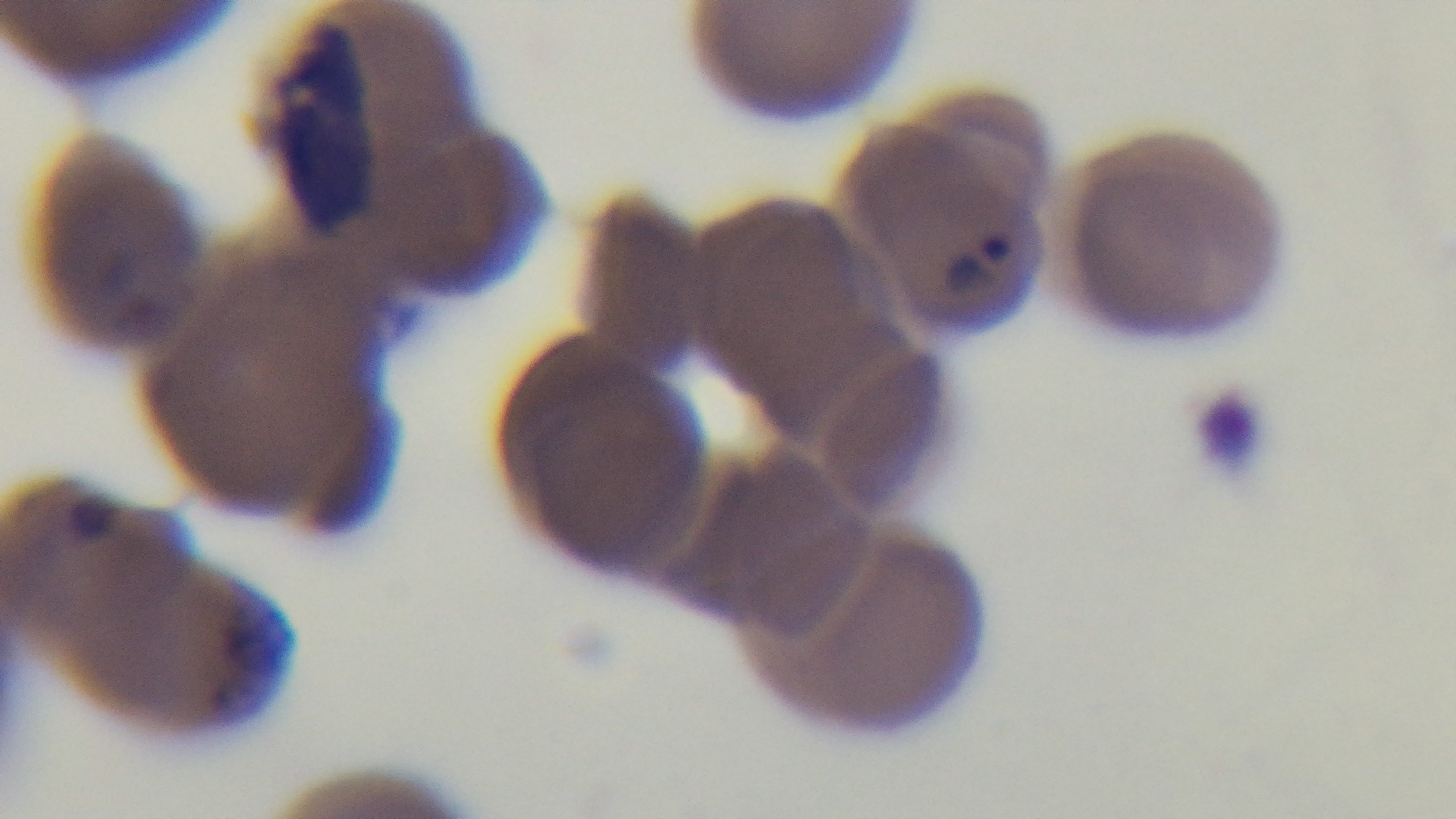

Photomicrograph. One field from the slide. Malaria status: positive. Giemsa stain. Preparation: thin. Mounted 4K digital camera. 100x oil-immersion objective.